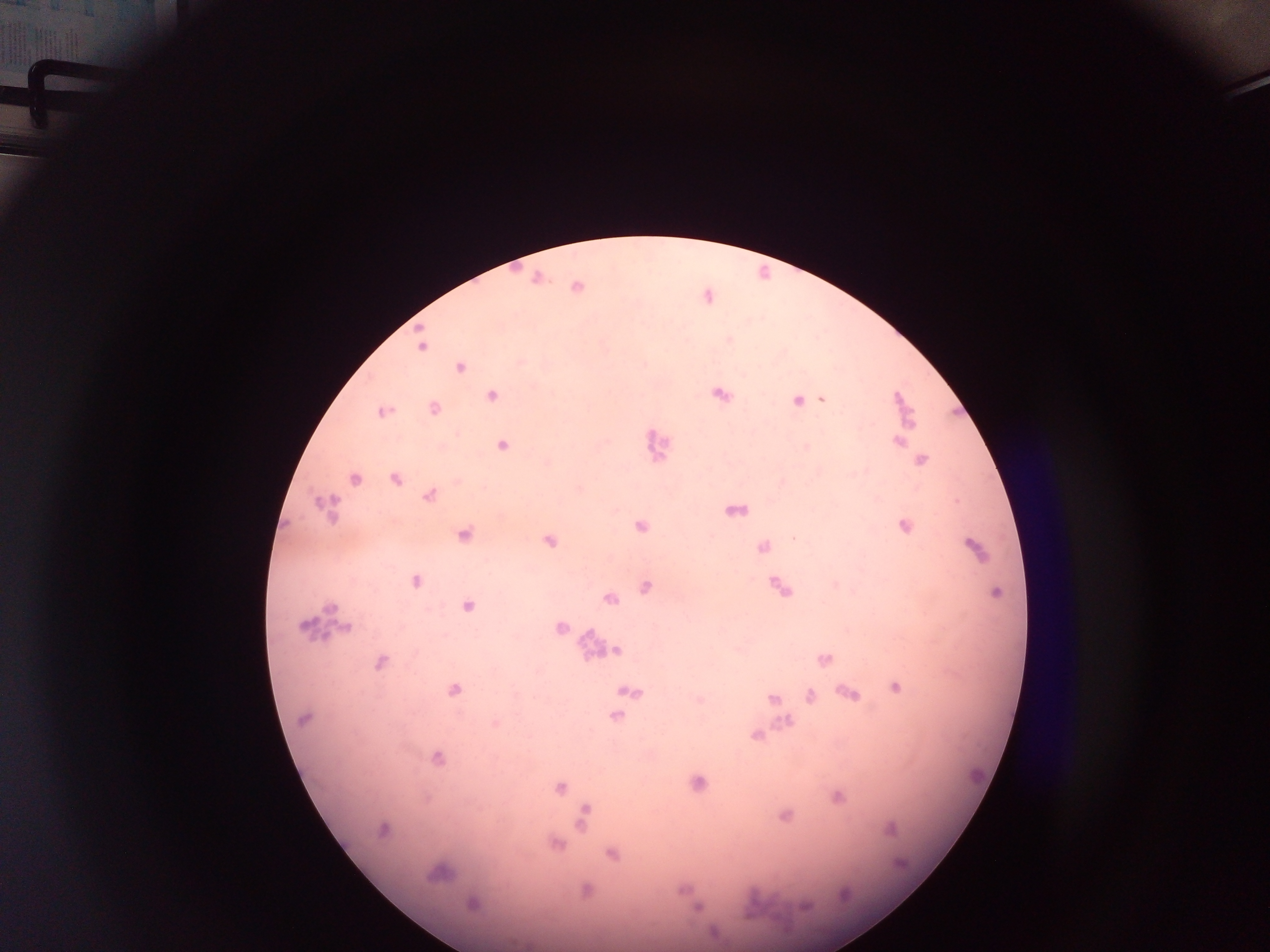 Approximate centers as x y in pixels. Malaria parasite locations: 421 347; 461 367; 491 395; 720 395; 821 400; 797 401; 433 408; 382 412; 899 442; 503 445; 921 460; 354 478; 395 479; 429 495; 325 507; 640 527; 904 527; 464 535; 794 538; 549 541; 763 547; 974 548; 416 581; 647 587; 997 592; 609 598; 467 607; 559 627; 618 650; 825 659; 380 662; 895 687; 454 690; 630 692; 850 693; 810 695; 773 698; 616 716; 304 718; 788 721; 495 723; 756 736; 438 758; 698 783; 560 787; 837 797; 783 815; 582 817; 382 829; 891 829; 556 844; 613 854; 438 874; 473 904; 805 906; 698 908. Leukocyte locations: 658 445; 326 621; 587 645; 978 775; 765 903. Mobile-phone photograph taken through the microscope. Thick blood smear. Single field of view. Image is 1270×952 pixels. Collected in Ghana.